Report the malaria status of this cell.
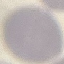
Uninfected.

Photographed with a smartphone camera at the microscope eyepiece. Cell patch, automatically extracted from a larger field of view and resized to 64 × 64 pixels. Giemsa stain. Thin smear of blood.